Comment on the morphology of the erythrocytes.
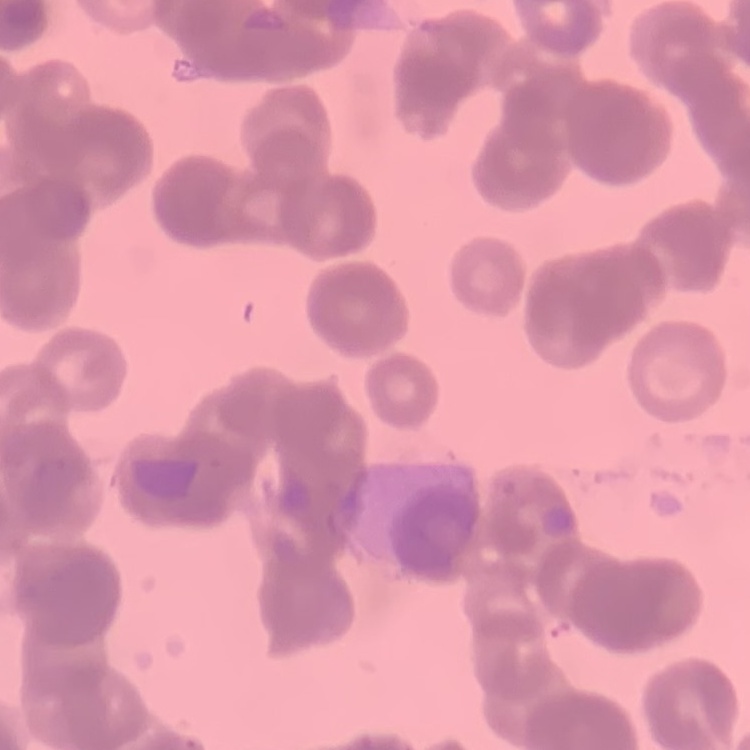

Rouleaux formation.

{
  "image_type": "one tile cut from a larger photomicrograph",
  "stain": "Field's or Giemsa",
  "preparation": "thin blood smear"
}